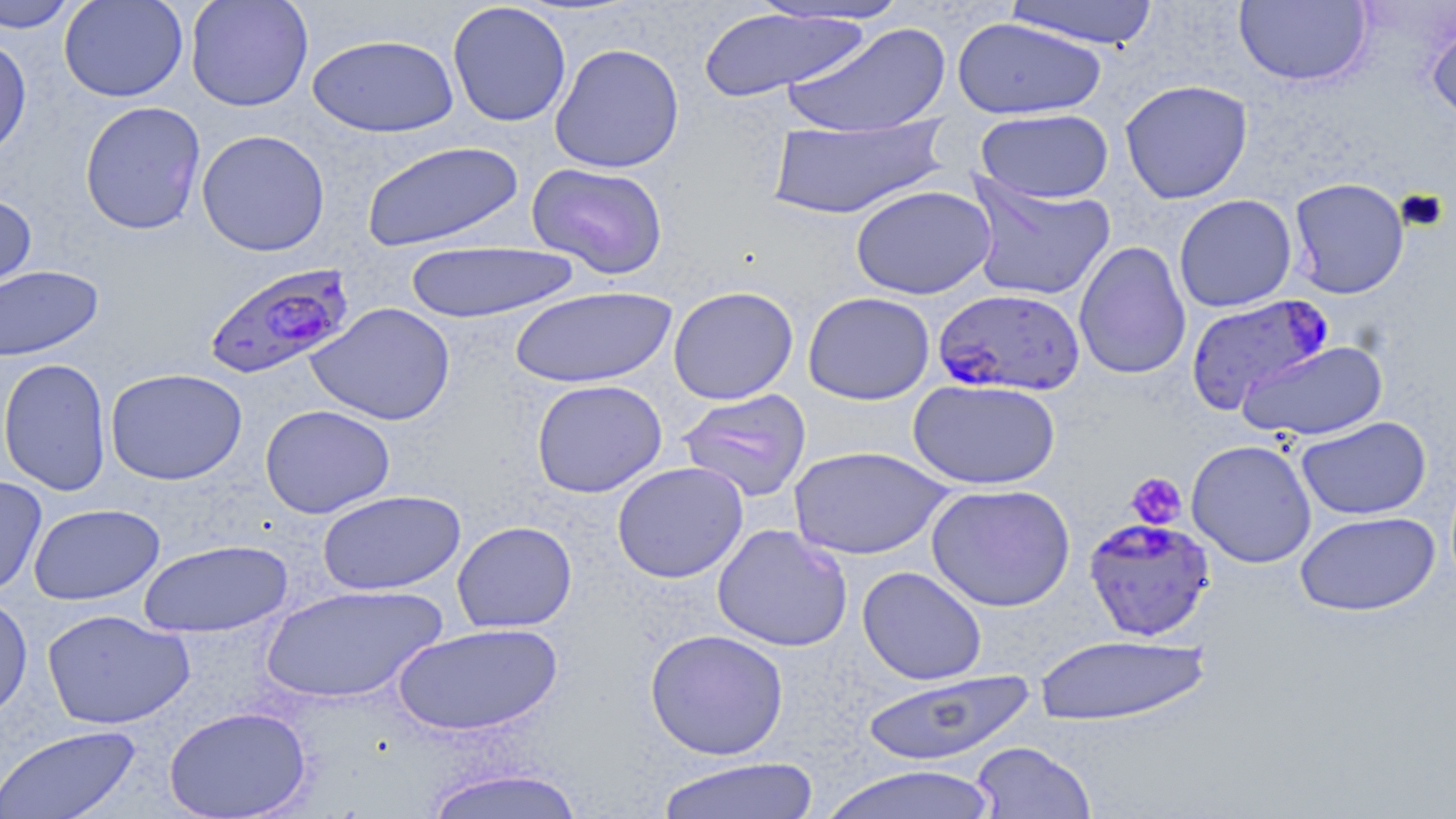

Approximate bounding boxes as (x1, y1, x2, y2) in pixels. Platelet locations: (1125, 472, 1187, 529). Uninfected red blood cell locations: (0, 0, 80, 32), (59, 0, 188, 102), (185, 0, 313, 112), (745, 0, 911, 26), (1003, 0, 1161, 48), (1234, 1, 1372, 88), (447, 2, 572, 127), (699, 7, 868, 102), (1425, 11, 1456, 128), (952, 17, 1106, 120), (781, 20, 953, 138), (307, 33, 459, 137), (0, 37, 33, 162), (549, 43, 685, 174), (1120, 79, 1253, 204), (79, 100, 206, 235), (975, 108, 1114, 203), (764, 116, 950, 220), (196, 129, 330, 256), (361, 140, 524, 252), (526, 162, 669, 279), (965, 175, 1115, 302), (1288, 177, 1410, 299), (850, 184, 997, 300), (0, 191, 37, 299), (1173, 194, 1297, 313), (1074, 240, 1192, 380), (403, 241, 580, 323), (0, 265, 103, 362), (668, 285, 799, 404), (508, 286, 676, 388), (803, 291, 935, 405), (307, 302, 455, 426), (1237, 340, 1388, 441), (0, 357, 112, 496), (105, 367, 248, 485), (907, 378, 1062, 490), (531, 379, 667, 498), (676, 388, 812, 502), (260, 404, 395, 518), (1295, 416, 1431, 520), (1186, 438, 1317, 568), (788, 445, 953, 560), (612, 461, 749, 583), (0, 475, 47, 598), (925, 483, 1076, 612), (316, 489, 466, 596), (28, 503, 164, 605), (1295, 511, 1440, 616), (451, 521, 578, 633), (712, 523, 852, 652), (137, 539, 293, 637), (857, 566, 987, 685), (259, 583, 448, 704), (0, 592, 34, 724), (41, 608, 194, 729), (392, 622, 563, 737), (645, 629, 789, 760), (1033, 633, 1212, 727), (859, 670, 1036, 766), (163, 705, 312, 818), (0, 725, 142, 818), (969, 741, 1096, 818), (655, 756, 820, 819), (819, 764, 1001, 819), (421, 766, 585, 819). Plasmodium falciparum-infected red blood cell locations: (202, 261, 356, 379), (932, 288, 1085, 397), (1183, 294, 1334, 416), (1083, 516, 1217, 642). Slide-level diagnosis: Plasmodium falciparum. 1000x magnification. Single field of view. May-Grünwald-Giemsa-stained preparation. Light microscopy. Thin blood smear. Image is 1456×819 pixels.